Assess the morphology of the red blood cells.
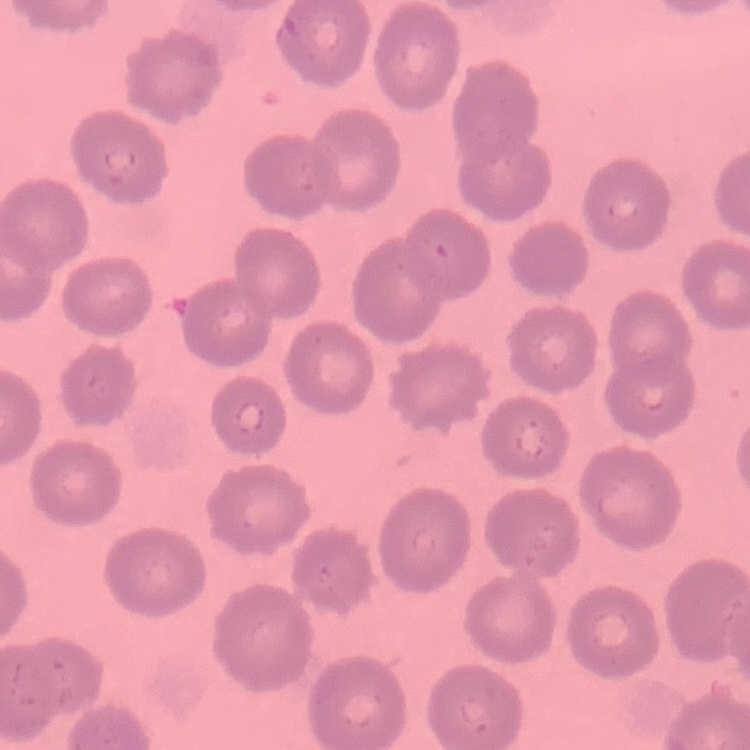

They show no rouleaux formation.

Stained with either Field's or Giemsa. Thin peripheral smear. Square crop of a larger photomicrograph.